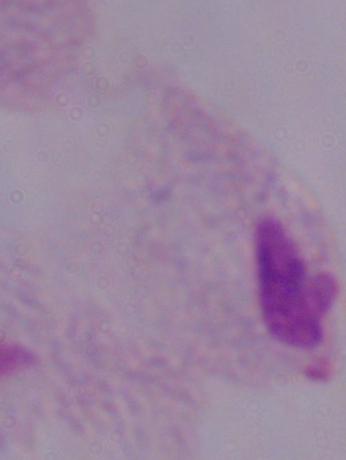

1000x magnification. A trichomonad is seen. Photomicrograph.